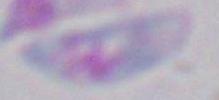

magnification = 1000x
identification = Toxoplasma gondii
modality = photomicrograph